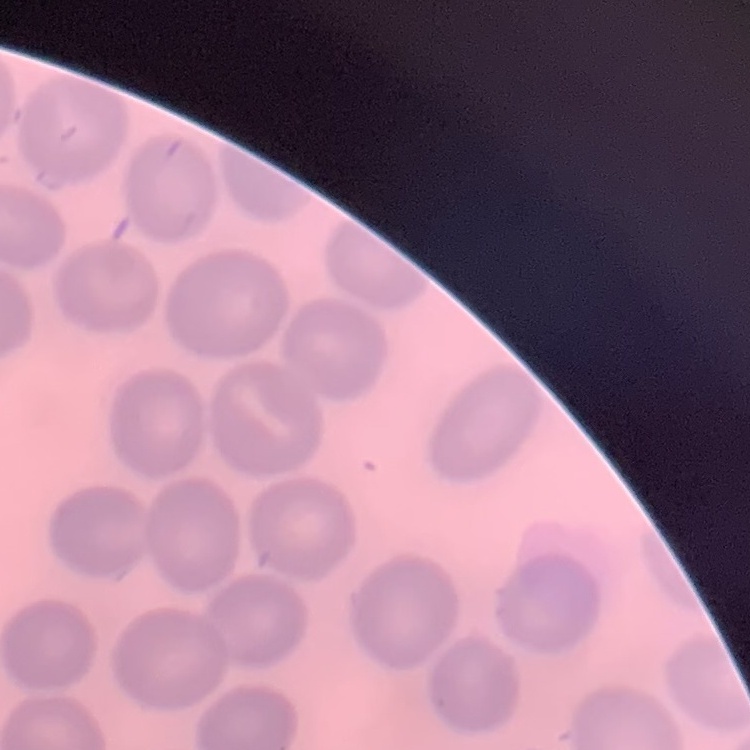
{
  "erythrocyte_morphology": "no rouleaux formation",
  "preparation": "thin blood film",
  "stain": "Field's or Giemsa",
  "image_type": "square crop of a larger photomicrograph"
}